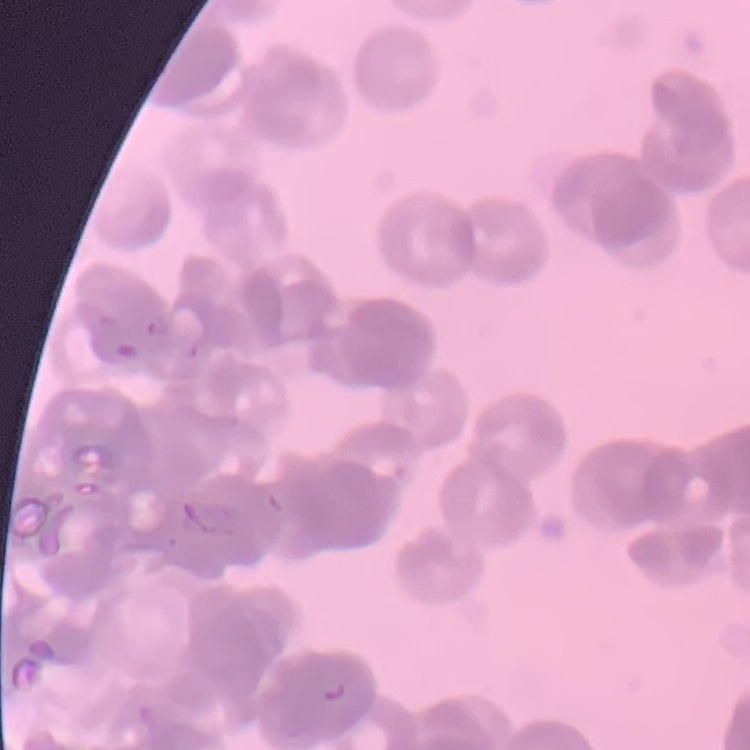

{
  "erythrocyte_morphology": "rouleaux formation",
  "image_type": "one tile cut from a larger photomicrograph",
  "preparation": "thin blood smear",
  "stain": "Field's or Giemsa"
}